Locate and identify every blood parasite.
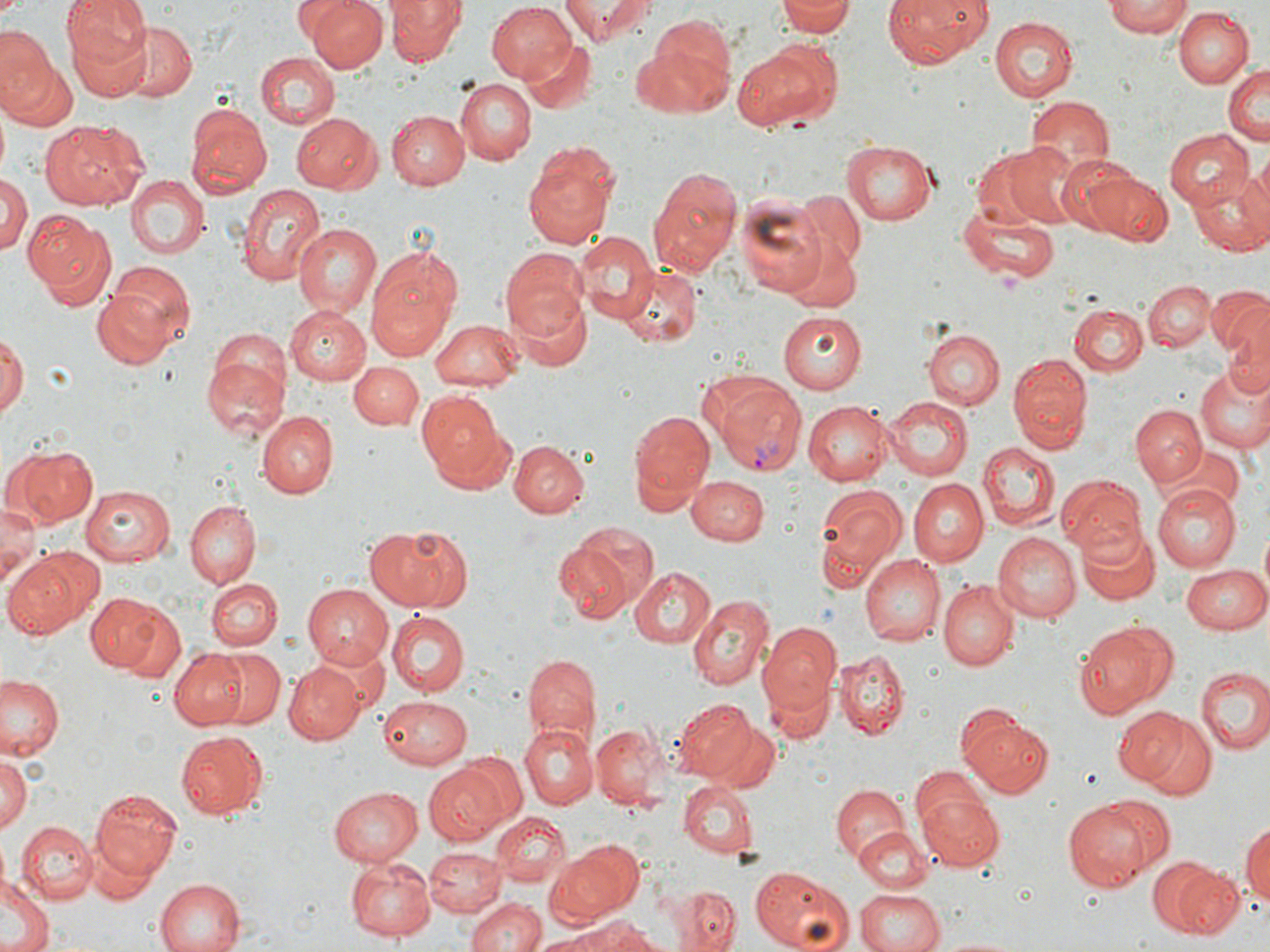

Approximate bounding boxes as named x1/y1/x2/y2 corners in pixels.
Plasmodium vivax-infected red blood cells: (x1=709, y1=377, x2=808, y2=476).
No Plasmodium falciparum, Plasmodium ovale, Plasmodium malariae, Babesia divergens, or Trypanosoma brucei observed.

Uninfected red blood cell locations: (x1=59, y1=0, x2=152, y2=96), (x1=306, y1=0, x2=385, y2=70), (x1=559, y1=0, x2=655, y2=44), (x1=884, y1=0, x2=993, y2=67), (x1=1104, y1=0, x2=1194, y2=39), (x1=387, y1=1, x2=465, y2=66), (x1=777, y1=1, x2=858, y2=37), (x1=485, y1=2, x2=578, y2=83), (x1=1173, y1=7, x2=1252, y2=86), (x1=989, y1=17, x2=1080, y2=102), (x1=639, y1=19, x2=735, y2=115), (x1=128, y1=24, x2=198, y2=102), (x1=0, y1=26, x2=54, y2=108), (x1=523, y1=37, x2=596, y2=113), (x1=735, y1=44, x2=836, y2=131), (x1=254, y1=52, x2=340, y2=130), (x1=0, y1=53, x2=75, y2=133), (x1=1224, y1=64, x2=1269, y2=147), (x1=457, y1=77, x2=536, y2=165), (x1=1026, y1=98, x2=1115, y2=179), (x1=184, y1=105, x2=271, y2=198), (x1=389, y1=110, x2=470, y2=188), (x1=291, y1=112, x2=380, y2=193), (x1=40, y1=120, x2=146, y2=209), (x1=1163, y1=129, x2=1254, y2=209), (x1=842, y1=138, x2=941, y2=226), (x1=1001, y1=141, x2=1085, y2=227), (x1=522, y1=154, x2=621, y2=248), (x1=1238, y1=154, x2=1270, y2=248), (x1=1066, y1=161, x2=1174, y2=248), (x1=647, y1=165, x2=743, y2=275), (x1=1189, y1=172, x2=1270, y2=255), (x1=0, y1=173, x2=30, y2=256), (x1=125, y1=175, x2=208, y2=260), (x1=234, y1=182, x2=326, y2=287), (x1=797, y1=191, x2=867, y2=266), (x1=736, y1=194, x2=831, y2=298), (x1=962, y1=202, x2=1061, y2=282), (x1=26, y1=214, x2=114, y2=310), (x1=293, y1=222, x2=382, y2=319), (x1=571, y1=232, x2=659, y2=325), (x1=780, y1=232, x2=864, y2=314), (x1=501, y1=249, x2=590, y2=340), (x1=367, y1=250, x2=457, y2=360), (x1=102, y1=262, x2=196, y2=357), (x1=616, y1=265, x2=703, y2=349), (x1=1144, y1=280, x2=1213, y2=352), (x1=504, y1=282, x2=593, y2=372), (x1=1207, y1=285, x2=1270, y2=365), (x1=92, y1=291, x2=173, y2=369), (x1=1070, y1=304, x2=1145, y2=374), (x1=283, y1=306, x2=370, y2=384), (x1=778, y1=312, x2=867, y2=394), (x1=1224, y1=316, x2=1270, y2=399), (x1=429, y1=320, x2=526, y2=391), (x1=923, y1=330, x2=1002, y2=410), (x1=1, y1=334, x2=25, y2=423), (x1=201, y1=343, x2=289, y2=442), (x1=1009, y1=354, x2=1092, y2=451), (x1=350, y1=360, x2=424, y2=428), (x1=1194, y1=365, x2=1270, y2=453), (x1=418, y1=391, x2=505, y2=481), (x1=883, y1=396, x2=971, y2=480), (x1=803, y1=399, x2=894, y2=482), (x1=1131, y1=405, x2=1206, y2=485), (x1=627, y1=406, x2=715, y2=513), (x1=256, y1=409, x2=337, y2=499), (x1=507, y1=439, x2=587, y2=518), (x1=979, y1=442, x2=1057, y2=529), (x1=9, y1=445, x2=98, y2=528), (x1=1058, y1=474, x2=1146, y2=557), (x1=687, y1=475, x2=768, y2=547), (x1=907, y1=478, x2=987, y2=566), (x1=1153, y1=484, x2=1242, y2=570), (x1=81, y1=485, x2=175, y2=565), (x1=815, y1=486, x2=907, y2=583), (x1=0, y1=501, x2=40, y2=588), (x1=186, y1=501, x2=259, y2=586), (x1=570, y1=519, x2=661, y2=608), (x1=365, y1=525, x2=469, y2=612), (x1=1078, y1=526, x2=1159, y2=606), (x1=993, y1=533, x2=1081, y2=623), (x1=556, y1=541, x2=636, y2=623), (x1=4, y1=548, x2=96, y2=639), (x1=860, y1=555, x2=945, y2=647), (x1=1180, y1=561, x2=1269, y2=633), (x1=630, y1=567, x2=716, y2=648), (x1=206, y1=578, x2=283, y2=650), (x1=938, y1=580, x2=1019, y2=670), (x1=303, y1=584, x2=398, y2=669), (x1=85, y1=591, x2=170, y2=673), (x1=686, y1=592, x2=773, y2=690), (x1=111, y1=604, x2=187, y2=685), (x1=388, y1=611, x2=469, y2=697), (x1=756, y1=622, x2=843, y2=719), (x1=1072, y1=622, x2=1175, y2=719), (x1=318, y1=638, x2=389, y2=713), (x1=171, y1=648, x2=251, y2=730), (x1=836, y1=649, x2=909, y2=737), (x1=211, y1=650, x2=285, y2=726), (x1=522, y1=653, x2=600, y2=744), (x1=283, y1=661, x2=364, y2=743), (x1=1196, y1=665, x2=1270, y2=752), (x1=761, y1=667, x2=834, y2=746), (x1=0, y1=675, x2=65, y2=760), (x1=377, y1=693, x2=472, y2=769), (x1=674, y1=698, x2=760, y2=782), (x1=1112, y1=707, x2=1191, y2=785), (x1=1137, y1=715, x2=1218, y2=801), (x1=961, y1=716, x2=1054, y2=798), (x1=590, y1=721, x2=667, y2=807), (x1=708, y1=721, x2=781, y2=791), (x1=520, y1=724, x2=597, y2=809), (x1=176, y1=730, x2=267, y2=820), (x1=0, y1=749, x2=31, y2=830), (x1=453, y1=749, x2=526, y2=829), (x1=423, y1=763, x2=515, y2=843), (x1=912, y1=767, x2=994, y2=840), (x1=678, y1=781, x2=759, y2=858), (x1=327, y1=785, x2=423, y2=866), (x1=830, y1=786, x2=906, y2=862), (x1=89, y1=789, x2=181, y2=882), (x1=917, y1=793, x2=1004, y2=868), (x1=1092, y1=796, x2=1177, y2=879), (x1=1063, y1=802, x2=1154, y2=893), (x1=492, y1=811, x2=570, y2=888), (x1=15, y1=821, x2=97, y2=905), (x1=1241, y1=821, x2=1270, y2=910), (x1=857, y1=826, x2=934, y2=892), (x1=544, y1=839, x2=644, y2=928), (x1=424, y1=847, x2=507, y2=917), (x1=90, y1=848, x2=153, y2=905), (x1=344, y1=853, x2=435, y2=940), (x1=1156, y1=859, x2=1240, y2=938), (x1=748, y1=865, x2=854, y2=952), (x1=0, y1=875, x2=53, y2=952), (x1=153, y1=878, x2=244, y2=951), (x1=666, y1=886, x2=742, y2=952), (x1=856, y1=887, x2=945, y2=952), (x1=466, y1=894, x2=543, y2=952), (x1=573, y1=918, x2=658, y2=952), (x1=607, y1=924, x2=675, y2=952), (x1=535, y1=926, x2=633, y2=951), (x1=933, y1=934, x2=1030, y2=952). Slide-level diagnosis: Plasmodium vivax. One field of a larger specimen. May-Grünwald-Giemsa-stained preparation. Optical microscopy. Image is 1270×952 pixels. 1000x magnification. Thin blood smear.